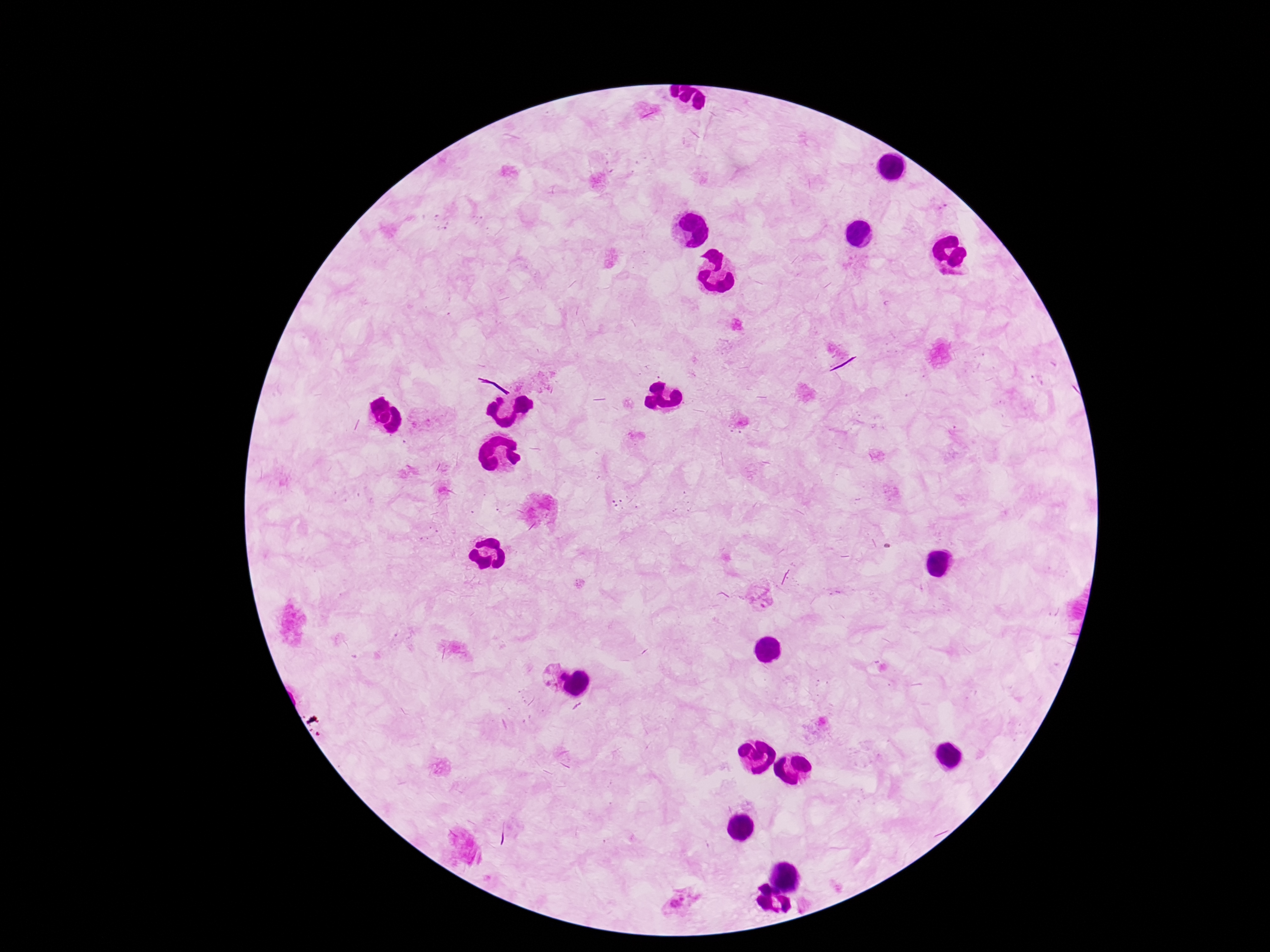
Plasmodium parasite locations = approximate centers as {x, y} in pixels: {941, 207}, {761, 594}, {547, 674}, {565, 677}, {682, 901}
patient malaria status = positive
preparation = thick blood film
image size = 1270×952 pixels
stain = Giemsa
field of view = single
capture = smartphone camera through the microscope eyepiece
magnification = 100x